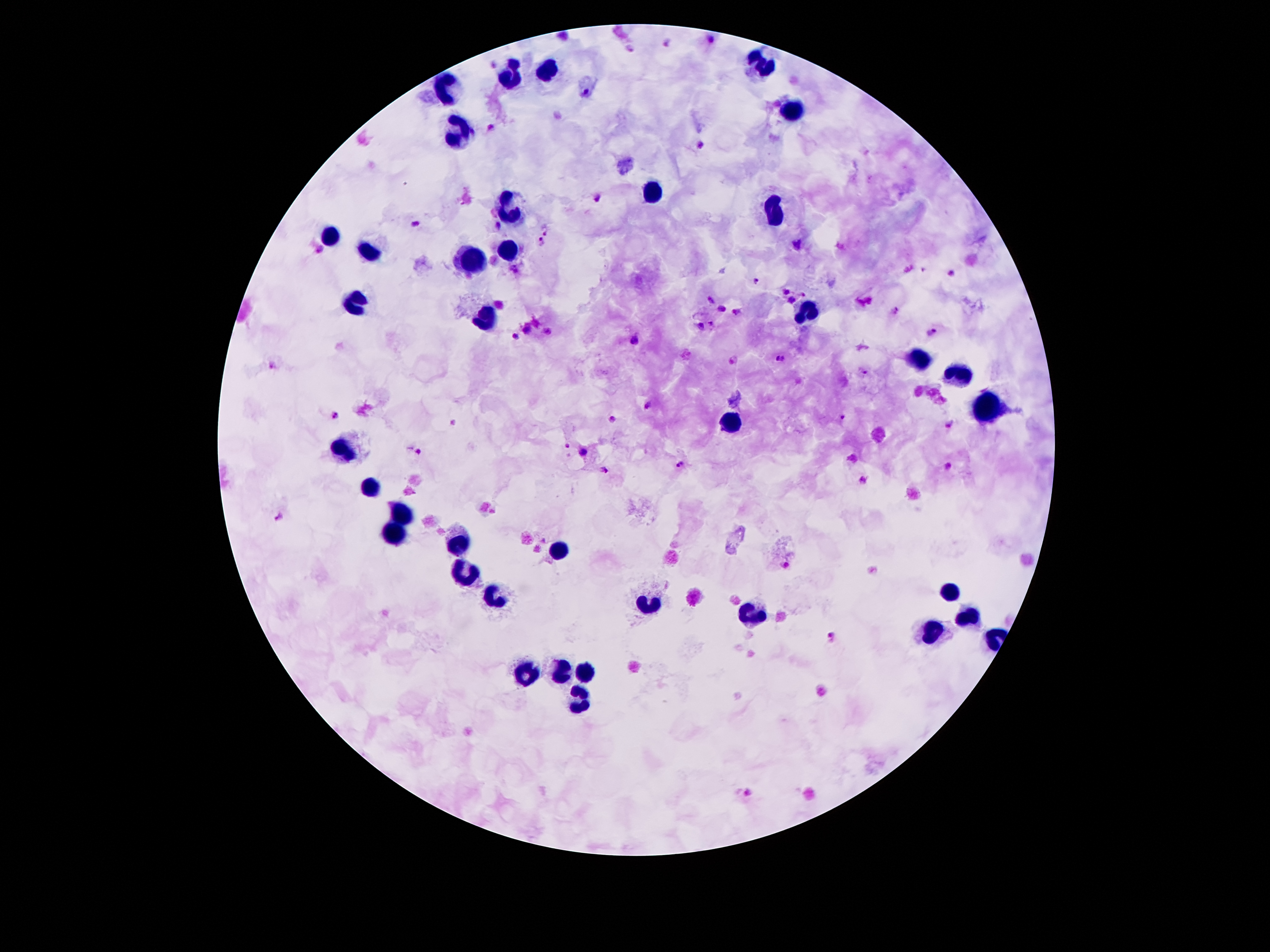

Approximate object centers, in pixels from the top-left corner. Malaria parasite locations: (x=712, y=38), (x=668, y=42), (x=495, y=64), (x=490, y=127), (x=700, y=146), (x=598, y=198), (x=417, y=222), (x=499, y=225), (x=545, y=230), (x=541, y=242), (x=515, y=269), (x=922, y=269), (x=952, y=274), (x=755, y=280), (x=786, y=293), (x=805, y=294), (x=793, y=299), (x=709, y=302), (x=722, y=308), (x=736, y=310), (x=897, y=310), (x=711, y=322), (x=701, y=327), (x=549, y=330), (x=525, y=331), (x=931, y=331), (x=515, y=336), (x=635, y=339), (x=732, y=359), (x=780, y=359), (x=271, y=366), (x=862, y=374), (x=648, y=405), (x=336, y=414), (x=843, y=416), (x=613, y=421), (x=949, y=426), (x=567, y=445), (x=418, y=452), (x=583, y=453), (x=853, y=458), (x=678, y=464), (x=949, y=466), (x=606, y=470), (x=864, y=479), (x=279, y=514), (x=786, y=565), (x=831, y=636). Leukocyte locations: (x=764, y=64), (x=555, y=69), (x=510, y=79), (x=450, y=86), (x=794, y=113), (x=456, y=134), (x=650, y=193), (x=508, y=204), (x=776, y=214), (x=331, y=233), (x=508, y=251), (x=370, y=254), (x=473, y=260), (x=356, y=305), (x=808, y=314), (x=484, y=321), (x=918, y=359), (x=960, y=375), (x=983, y=408), (x=731, y=420), (x=345, y=452), (x=372, y=483), (x=401, y=515), (x=397, y=531), (x=460, y=544), (x=556, y=546), (x=467, y=576), (x=947, y=591), (x=498, y=597), (x=651, y=607), (x=753, y=615), (x=966, y=620), (x=932, y=633), (x=588, y=668), (x=561, y=672), (x=528, y=673), (x=580, y=699). 100x magnification. Image is 1270×952 pixels. Giemsa-stained preparation. Smartphone photograph taken through the microscope eyepiece. Single field of view. Thick peripheral-blood smear. Patient malaria status: infected with Plasmodium falciparum.